State which cell type is depicted.
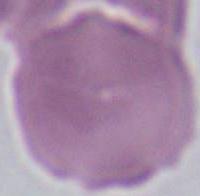

An erythrocyte.

modality: photomicrograph
magnification: 1000x